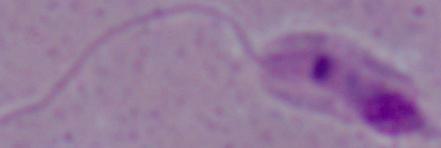

magnification: 1000x
modality: photomicrograph
identification: Leishmania